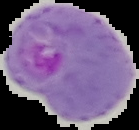

From a thin blood film. Segmented cell region on a black background. Image is 139×130 pixels. Result: Plasmodium parasites detected.